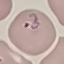
Summary:
  - Malaria status: parasitized
  - Image type: automatically extracted cell patch, resized to 64 × 64 pixels
  - Stain: Giemsa
  - Capture: smartphone through the microscope eyepiece
  - Preparation: thin smear